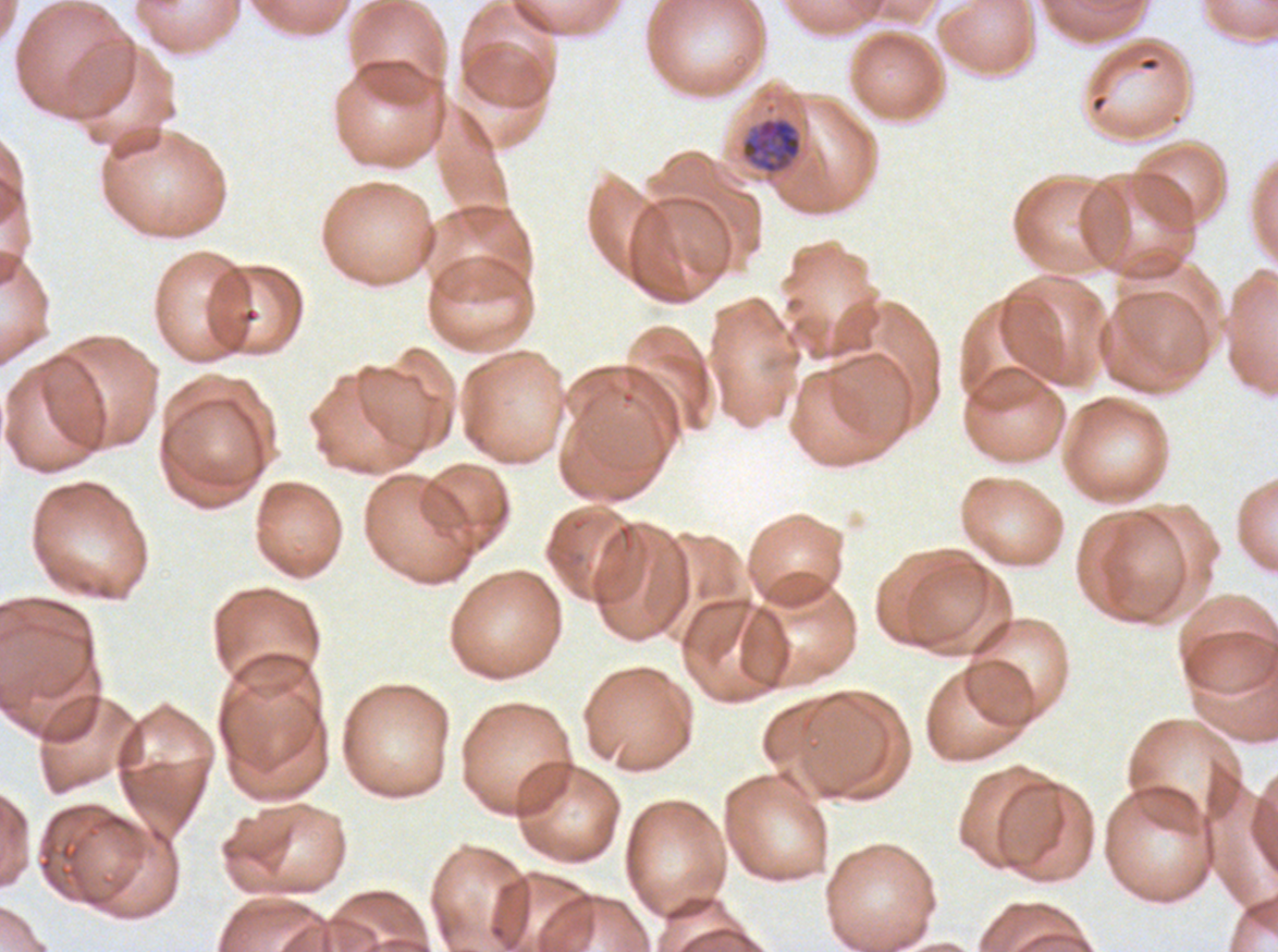
notation = approximate bounding boxes as [x1, y1, x2, y2] in pixels
mid trophozoite locations = [741, 117, 802, 175]
image size = 1278×952 pixels
field of view = one sub-image of a larger composite
specimen = ex-vivo Plasmodium falciparum culture from a patient in The Gambia, grown for 24 to 48 hours
stain = Giemsa
preparation = thin blood smear